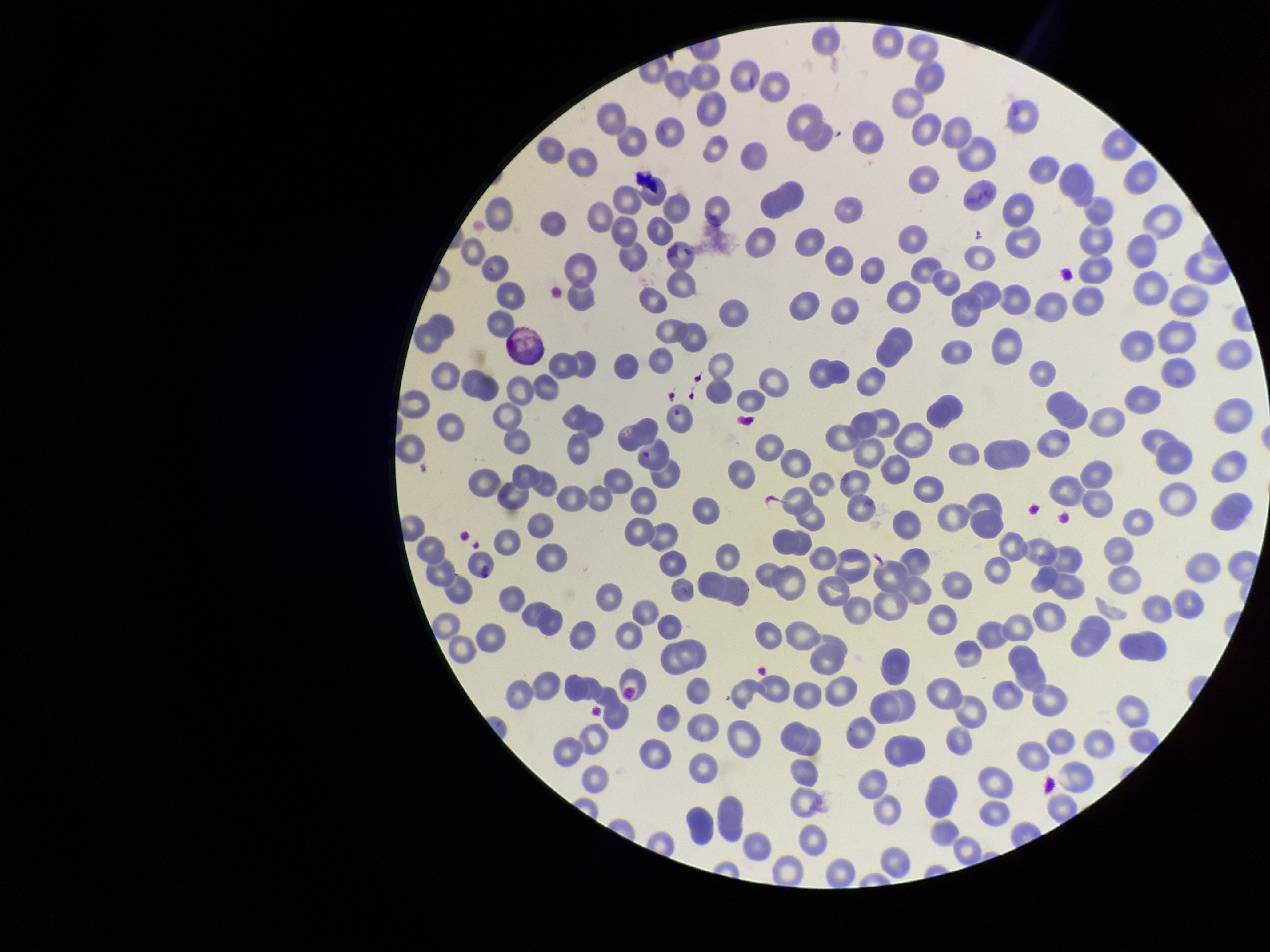

Summary:
  - Species reported for this patient: Plasmodium vivax
  - Parasitized red blood cell count: 0
  - Preparation: thin blood smear
  - Field of view: single
  - Red blood cell count: 229
  - Image size: 1270×952 pixels
  - Stain: Giemsa
  - Capture: smartphone photograph through the microscope eyepiece
  - Parasitized red blood cells: none seen
  - Patient malaria status: positive